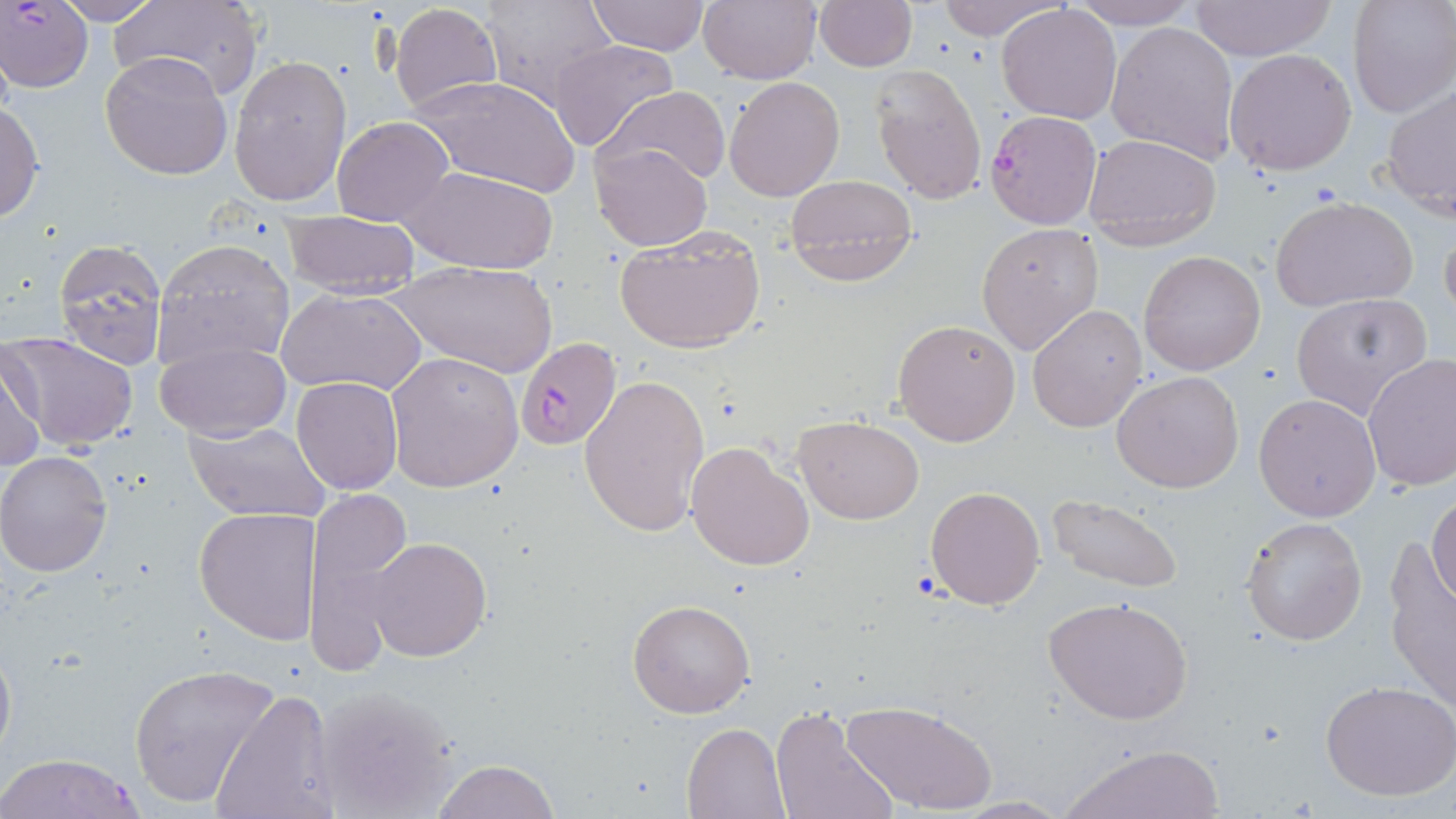

Summary:
  - Coordinate format: approximate bounding boxes as (x1, y1, x2, y2) in pixels
  - Plasmodium falciparum-infected red blood cell locations: (1, 1, 92, 95), (985, 110, 1100, 229), (515, 339, 622, 449), (1, 753, 148, 818)
  - Uninfected red blood cell locations: (51, 0, 165, 25), (109, 0, 264, 100), (480, 0, 620, 109), (584, 0, 827, 67), (585, 0, 712, 56), (698, 0, 819, 83), (931, 0, 1068, 40), (1065, 0, 1201, 28), (1187, 0, 1340, 62), (1346, 0, 1456, 119), (389, 2, 503, 118), (814, 2, 917, 71), (997, 5, 1122, 124), (1106, 20, 1240, 164), (547, 39, 679, 154), (1225, 47, 1357, 176), (227, 51, 350, 208), (99, 52, 234, 181), (869, 65, 988, 204), (409, 74, 580, 196), (723, 76, 845, 201), (599, 86, 731, 186), (1380, 87, 1456, 220), (0, 101, 44, 223), (332, 116, 453, 226), (1082, 133, 1222, 248), (591, 142, 713, 251), (405, 166, 557, 275), (784, 174, 919, 284), (1270, 196, 1418, 314), (284, 211, 420, 299), (977, 223, 1104, 357), (1440, 225, 1456, 329), (613, 227, 767, 354), (52, 238, 169, 368), (153, 240, 294, 370), (1138, 250, 1266, 376), (391, 260, 557, 377), (279, 286, 426, 398), (1291, 295, 1431, 420), (1027, 303, 1147, 432), (892, 318, 1021, 447), (1, 331, 140, 454), (156, 340, 291, 441), (0, 344, 48, 475), (386, 350, 525, 491), (1363, 355, 1456, 491), (579, 371, 711, 540), (1112, 371, 1244, 494), (292, 376, 404, 494), (1253, 393, 1382, 521), (794, 416, 924, 524), (185, 421, 332, 523), (686, 441, 816, 572), (1, 451, 114, 576), (925, 485, 1046, 611), (302, 490, 412, 673), (1046, 491, 1183, 596), (1429, 495, 1456, 606), (193, 508, 321, 646), (1240, 515, 1368, 646), (368, 537, 491, 660), (1380, 544, 1455, 709), (1043, 596, 1194, 725), (627, 600, 754, 720), (0, 634, 16, 767), (127, 662, 280, 808), (1321, 681, 1456, 802), (308, 684, 464, 818), (210, 689, 338, 819), (841, 698, 995, 814), (771, 707, 896, 819), (682, 720, 791, 818), (1060, 742, 1226, 819), (432, 759, 560, 819), (947, 797, 1075, 817)
  - Slide-level diagnosis: Plasmodium falciparum
  - Modality: optical microscopy
  - Stain: May-Grünwald-Giemsa
  - Field of view: single
  - Magnification: 1000x
  - Image size: 1456×819 pixels
  - Preparation: thin blood smear